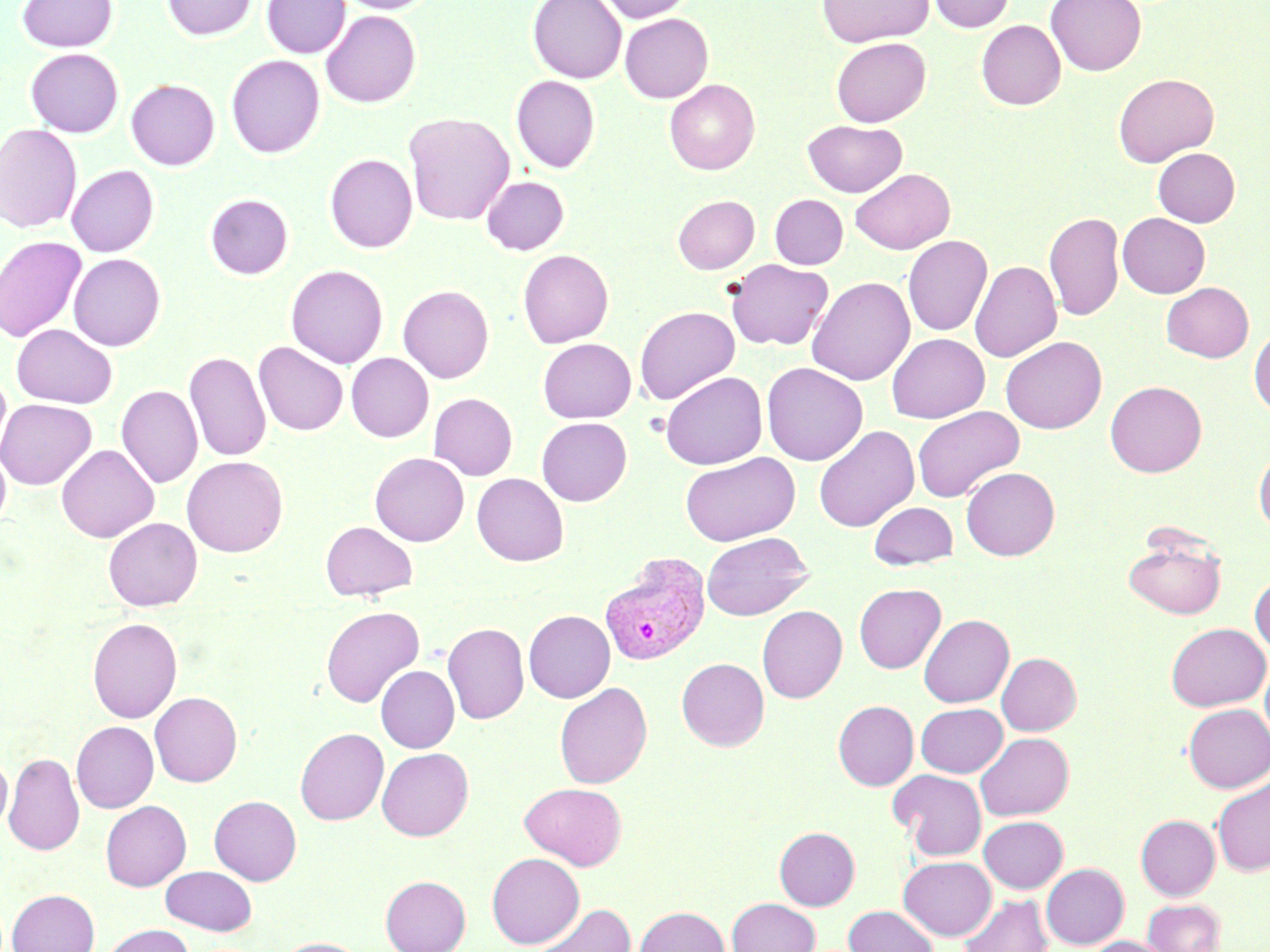 Approximate bounding boxes as named x1/y1/x2/y2 corners in pixels. Uninfected red blood cell locations: (x1=17, y1=0, x2=118, y2=52), (x1=162, y1=0, x2=256, y2=40), (x1=261, y1=0, x2=350, y2=58), (x1=335, y1=0, x2=436, y2=14), (x1=528, y1=0, x2=626, y2=82), (x1=597, y1=0, x2=696, y2=23), (x1=817, y1=0, x2=933, y2=47), (x1=928, y1=0, x2=1015, y2=33), (x1=1046, y1=0, x2=1147, y2=76), (x1=321, y1=10, x2=420, y2=108), (x1=620, y1=13, x2=713, y2=103), (x1=976, y1=20, x2=1065, y2=110), (x1=831, y1=37, x2=931, y2=127), (x1=25, y1=48, x2=123, y2=137), (x1=226, y1=55, x2=325, y2=158), (x1=1113, y1=73, x2=1219, y2=166), (x1=125, y1=74, x2=325, y2=164), (x1=511, y1=75, x2=600, y2=172), (x1=664, y1=78, x2=760, y2=175), (x1=126, y1=79, x2=220, y2=169), (x1=403, y1=112, x2=515, y2=226), (x1=803, y1=119, x2=907, y2=197), (x1=0, y1=124, x2=82, y2=232), (x1=1153, y1=148, x2=1240, y2=226), (x1=325, y1=153, x2=418, y2=253), (x1=66, y1=165, x2=159, y2=256), (x1=850, y1=168, x2=955, y2=255), (x1=481, y1=176, x2=569, y2=255), (x1=205, y1=193, x2=293, y2=279), (x1=672, y1=194, x2=760, y2=273), (x1=770, y1=194, x2=848, y2=269), (x1=1044, y1=211, x2=1124, y2=321), (x1=1117, y1=213, x2=1210, y2=298), (x1=0, y1=235, x2=86, y2=344), (x1=903, y1=235, x2=992, y2=336), (x1=518, y1=249, x2=614, y2=348), (x1=68, y1=253, x2=166, y2=351), (x1=725, y1=259, x2=833, y2=350), (x1=970, y1=260, x2=1062, y2=362), (x1=285, y1=264, x2=388, y2=368), (x1=806, y1=276, x2=915, y2=385), (x1=1161, y1=282, x2=1253, y2=362), (x1=398, y1=285, x2=494, y2=383), (x1=634, y1=305, x2=740, y2=405), (x1=12, y1=324, x2=117, y2=408), (x1=1249, y1=326, x2=1270, y2=416), (x1=886, y1=333, x2=989, y2=423), (x1=1000, y1=336, x2=1107, y2=434), (x1=537, y1=338, x2=637, y2=423), (x1=254, y1=342, x2=348, y2=436), (x1=184, y1=351, x2=271, y2=462), (x1=346, y1=353, x2=434, y2=442), (x1=761, y1=362, x2=868, y2=466), (x1=0, y1=369, x2=12, y2=466), (x1=660, y1=371, x2=767, y2=469), (x1=1105, y1=380, x2=1206, y2=477), (x1=116, y1=385, x2=203, y2=489), (x1=429, y1=393, x2=518, y2=480), (x1=0, y1=398, x2=98, y2=489), (x1=912, y1=406, x2=1024, y2=503), (x1=536, y1=417, x2=632, y2=506), (x1=813, y1=425, x2=919, y2=531), (x1=56, y1=444, x2=159, y2=542), (x1=1254, y1=444, x2=1270, y2=535), (x1=0, y1=445, x2=11, y2=531), (x1=370, y1=452, x2=469, y2=546), (x1=680, y1=452, x2=800, y2=546), (x1=182, y1=456, x2=288, y2=557), (x1=961, y1=467, x2=1060, y2=560), (x1=472, y1=473, x2=568, y2=566), (x1=868, y1=501, x2=957, y2=570), (x1=103, y1=517, x2=202, y2=611), (x1=321, y1=521, x2=417, y2=601), (x1=700, y1=532, x2=813, y2=621), (x1=1123, y1=532, x2=1227, y2=619), (x1=1250, y1=574, x2=1270, y2=657), (x1=854, y1=583, x2=946, y2=673), (x1=321, y1=605, x2=424, y2=707), (x1=757, y1=605, x2=847, y2=702), (x1=523, y1=610, x2=615, y2=702), (x1=918, y1=614, x2=1014, y2=707), (x1=87, y1=617, x2=182, y2=722), (x1=442, y1=622, x2=529, y2=724), (x1=1166, y1=623, x2=1269, y2=711), (x1=997, y1=652, x2=1081, y2=735), (x1=1260, y1=655, x2=1270, y2=748), (x1=676, y1=658, x2=769, y2=751), (x1=376, y1=665, x2=459, y2=752), (x1=554, y1=682, x2=653, y2=789), (x1=149, y1=691, x2=242, y2=787), (x1=833, y1=700, x2=919, y2=790), (x1=916, y1=703, x2=1007, y2=777), (x1=1183, y1=703, x2=1270, y2=793), (x1=71, y1=721, x2=159, y2=812), (x1=295, y1=727, x2=389, y2=825), (x1=975, y1=732, x2=1074, y2=820), (x1=377, y1=748, x2=473, y2=840), (x1=3, y1=752, x2=84, y2=856), (x1=0, y1=754, x2=12, y2=832), (x1=888, y1=769, x2=987, y2=860), (x1=1212, y1=778, x2=1270, y2=876), (x1=521, y1=782, x2=627, y2=869), (x1=209, y1=795, x2=302, y2=885), (x1=100, y1=800, x2=191, y2=890), (x1=1136, y1=814, x2=1220, y2=900), (x1=979, y1=816, x2=1068, y2=893), (x1=774, y1=826, x2=860, y2=910), (x1=486, y1=852, x2=585, y2=949), (x1=898, y1=856, x2=996, y2=941), (x1=1041, y1=863, x2=1129, y2=949), (x1=161, y1=865, x2=256, y2=935), (x1=380, y1=875, x2=470, y2=952), (x1=6, y1=889, x2=100, y2=952), (x1=958, y1=894, x2=1053, y2=952), (x1=727, y1=897, x2=820, y2=952), (x1=1143, y1=899, x2=1225, y2=952), (x1=530, y1=903, x2=637, y2=952), (x1=634, y1=905, x2=730, y2=952), (x1=844, y1=905, x2=938, y2=952), (x1=102, y1=924, x2=194, y2=952), (x1=1086, y1=935, x2=1172, y2=952), (x1=277, y1=937, x2=366, y2=952). Plasmodium vivax-infected red blood cell locations: (x1=599, y1=552, x2=710, y2=666). Slide-level diagnosis: Plasmodium vivax. Thin blood smear. 1000x magnification. Light microscopy. May-Grünwald-Giemsa stain. Single field of view. Image is 1270×952 pixels.